Locate and identify every blood parasite.
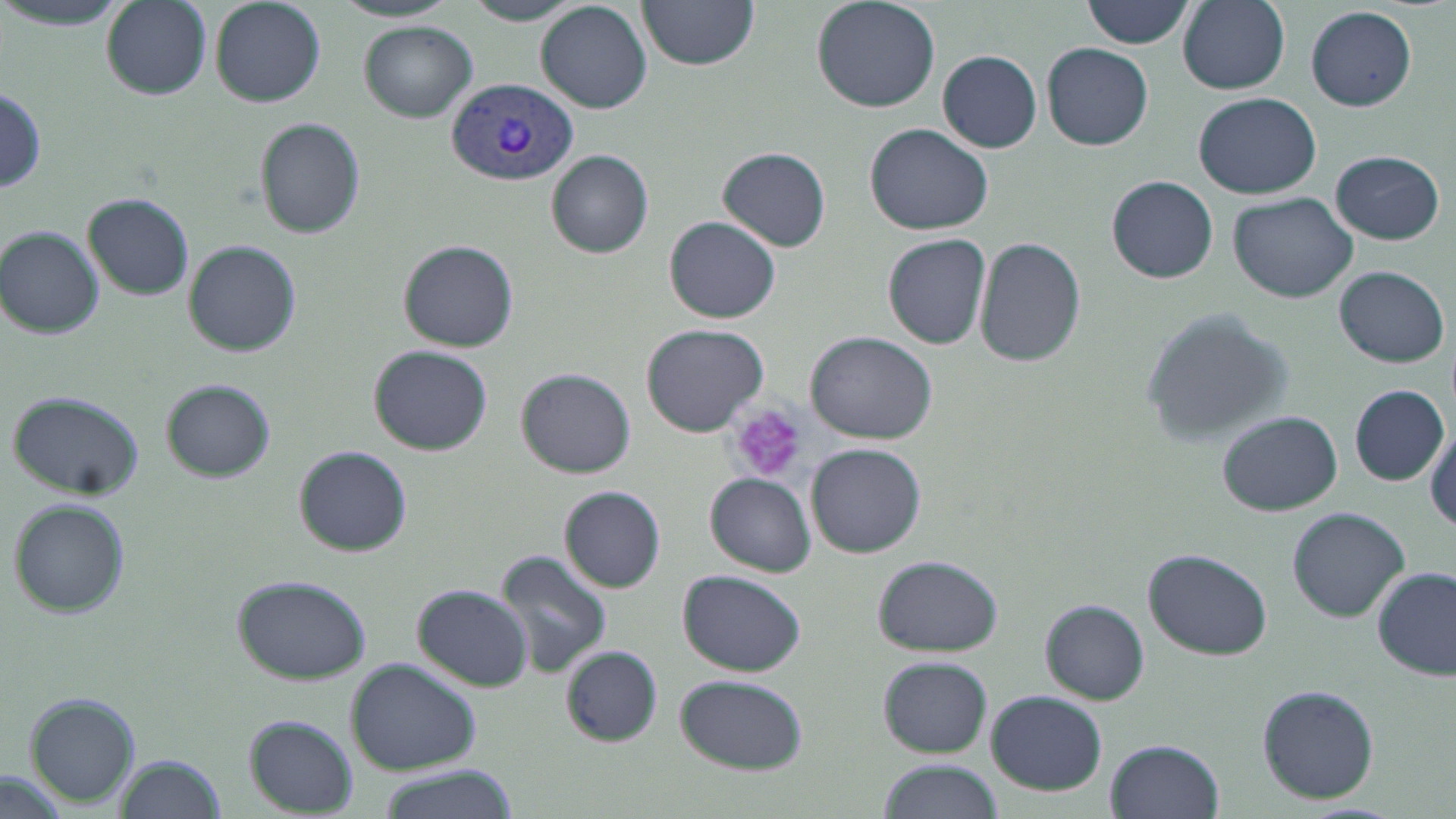
Approximate bounding boxes as named x1/y1/x2/y2 corners in pixels.
Plasmodium vivax-infected red blood cells: (x1=446, y1=78, x2=578, y2=184).
No Plasmodium falciparum, Plasmodium ovale, Plasmodium malariae, Babesia divergens, or Trypanosoma brucei observed.

Platelet locations: (x1=730, y1=401, x2=808, y2=483). Uninfected red blood cell locations: (x1=101, y1=0, x2=210, y2=99), (x1=637, y1=0, x2=761, y2=70), (x1=811, y1=0, x2=941, y2=114), (x1=1083, y1=0, x2=1196, y2=48), (x1=1177, y1=0, x2=1290, y2=93), (x1=0, y1=1, x2=130, y2=31), (x1=208, y1=1, x2=324, y2=107), (x1=335, y1=1, x2=458, y2=22), (x1=463, y1=1, x2=582, y2=25), (x1=536, y1=1, x2=651, y2=113), (x1=1304, y1=6, x2=1416, y2=112), (x1=360, y1=21, x2=477, y2=121), (x1=1042, y1=42, x2=1153, y2=150), (x1=937, y1=50, x2=1042, y2=153), (x1=1, y1=86, x2=47, y2=193), (x1=1194, y1=91, x2=1321, y2=199), (x1=253, y1=118, x2=366, y2=239), (x1=865, y1=123, x2=993, y2=235), (x1=717, y1=147, x2=830, y2=252), (x1=1330, y1=149, x2=1445, y2=244), (x1=547, y1=150, x2=653, y2=257), (x1=1107, y1=176, x2=1219, y2=284), (x1=1229, y1=191, x2=1357, y2=303), (x1=83, y1=192, x2=193, y2=300), (x1=666, y1=216, x2=779, y2=323), (x1=1, y1=227, x2=103, y2=338), (x1=882, y1=232, x2=991, y2=350), (x1=976, y1=238, x2=1085, y2=369), (x1=397, y1=240, x2=519, y2=352), (x1=185, y1=241, x2=302, y2=357), (x1=1334, y1=265, x2=1450, y2=367), (x1=1140, y1=310, x2=1297, y2=448), (x1=639, y1=323, x2=768, y2=436), (x1=806, y1=330, x2=939, y2=444), (x1=369, y1=345, x2=492, y2=455), (x1=516, y1=367, x2=635, y2=477), (x1=161, y1=379, x2=275, y2=482), (x1=1351, y1=384, x2=1448, y2=484), (x1=6, y1=390, x2=144, y2=499), (x1=1218, y1=410, x2=1344, y2=515), (x1=1425, y1=426, x2=1456, y2=536), (x1=807, y1=443, x2=925, y2=557), (x1=297, y1=445, x2=413, y2=555), (x1=706, y1=473, x2=814, y2=575), (x1=560, y1=484, x2=666, y2=593), (x1=8, y1=499, x2=130, y2=617), (x1=1287, y1=507, x2=1410, y2=622), (x1=1144, y1=548, x2=1274, y2=658), (x1=496, y1=550, x2=615, y2=677), (x1=873, y1=554, x2=1003, y2=655), (x1=1373, y1=566, x2=1456, y2=679), (x1=677, y1=570, x2=806, y2=675), (x1=230, y1=574, x2=371, y2=684), (x1=412, y1=584, x2=533, y2=693), (x1=1041, y1=600, x2=1149, y2=704), (x1=561, y1=647, x2=661, y2=745), (x1=879, y1=657, x2=993, y2=756), (x1=348, y1=659, x2=479, y2=773), (x1=677, y1=675, x2=807, y2=773), (x1=1256, y1=684, x2=1380, y2=804), (x1=987, y1=689, x2=1106, y2=796), (x1=25, y1=694, x2=139, y2=806), (x1=243, y1=715, x2=357, y2=813), (x1=1106, y1=739, x2=1224, y2=819), (x1=115, y1=756, x2=225, y2=819), (x1=876, y1=760, x2=1004, y2=818), (x1=373, y1=768, x2=518, y2=819). Slide-level diagnosis: Plasmodium vivax. Optical microscopy. Thin blood film. May-Grünwald-Giemsa stain. Image is 1456×819 pixels. 1000x magnification. One field of a larger specimen.